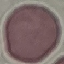 Malaria status: uninfected. Automatically extracted cell patch, resized to 64 × 64 pixels. Acquired by smartphone through the microscope eyepiece. Thin smear of blood. Giemsa-stained preparation.